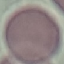

Summary:
  - Malaria status: uninfected
  - Stain: Giemsa
  - Capture: smartphone through the microscope eyepiece
  - Preparation: thin blood film
  - Image type: cell patch, automatically extracted from a larger field of view and resized to 64 × 64 pixels